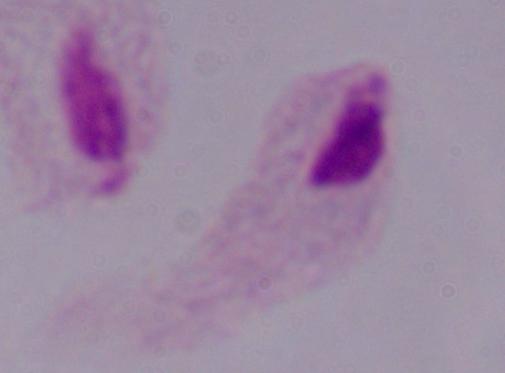

Summary:
  - Identification: trichomonad
  - Magnification: 1000x
  - Modality: photomicrograph